Outline platelets.
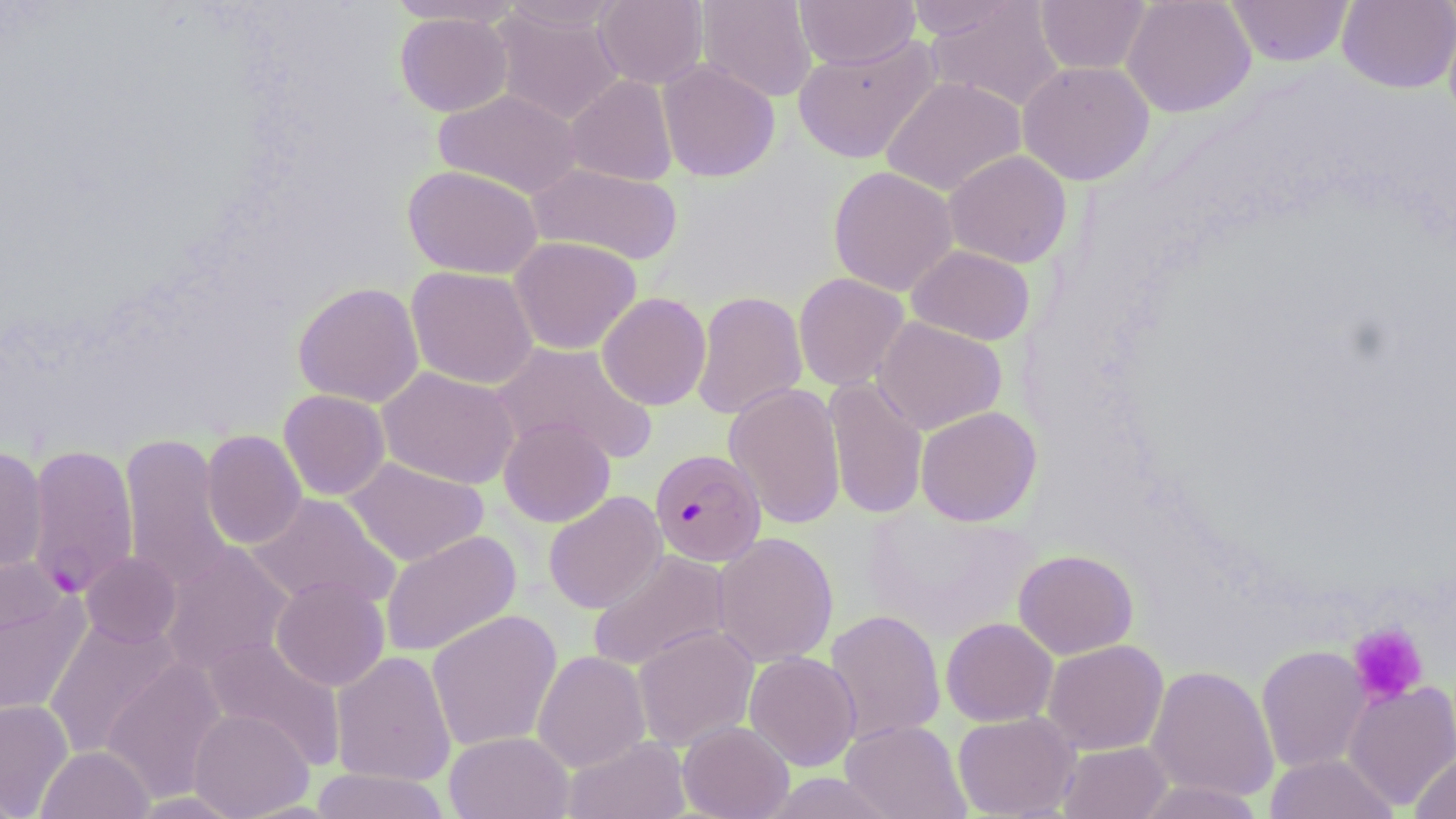
Approximate bounding boxes as [x1, y1, x2, y2] in pixels.
Platelets: [1347, 622, 1429, 706].

slide_level_diagnosis: Plasmodium falciparum
magnification: 1000x
image_size: 1456×819 pixels
modality: optical microscopy
field_of_view: one of a larger specimen
plasmodium_falciparum_infected_red_blood_cell_locations: 'approximate bounding boxes as [x1, y1, x2, y2] in pixels: [26, 443, 139, 597], [650, 448, 767, 566]'
stain: May-Grünwald-Giemsa
uninfected_red_blood_cell_locations: 'approximate bounding boxes as [x1, y1, x2, y2] in pixels: [385, 0, 523, 26], [593, 0, 708, 89], [696, 0, 817, 103], [794, 0, 920, 70], [904, 0, 1023, 40], [1034, 0, 1151, 75], [1121, 0, 1256, 117], [1225, 0, 1355, 67], [1337, 0, 1456, 94], [500, 1, 624, 31], [924, 1, 1066, 112], [490, 6, 624, 125], [395, 11, 513, 117], [792, 35, 942, 164], [657, 59, 780, 182], [1017, 60, 1155, 185], [565, 75, 678, 185], [881, 76, 1026, 196], [433, 88, 581, 198], [944, 150, 1072, 268], [526, 163, 684, 266], [403, 164, 542, 279], [828, 166, 958, 296], [509, 236, 642, 355], [907, 245, 1035, 345], [405, 266, 539, 389], [793, 272, 909, 391], [293, 282, 425, 407], [692, 290, 807, 421], [596, 292, 711, 410], [873, 316, 1007, 435], [491, 341, 658, 465], [377, 366, 521, 489], [824, 376, 928, 520], [724, 383, 847, 530], [278, 389, 390, 500], [915, 406, 1042, 527], [499, 417, 615, 527], [201, 430, 307, 550], [119, 433, 234, 592], [0, 445, 48, 573], [343, 457, 488, 567], [543, 491, 667, 614], [247, 492, 400, 611], [380, 530, 521, 657], [712, 531, 839, 668], [159, 543, 294, 675], [588, 548, 731, 673], [1013, 549, 1138, 659], [80, 551, 181, 648], [0, 553, 62, 649], [270, 576, 390, 691], [0, 596, 89, 719], [427, 609, 562, 753], [825, 609, 946, 745], [43, 617, 181, 760], [941, 617, 1058, 727], [633, 625, 759, 750], [202, 636, 347, 769], [1042, 640, 1168, 755], [1256, 645, 1371, 773], [332, 650, 456, 786], [532, 650, 650, 772], [744, 651, 861, 771], [101, 658, 228, 803], [1146, 664, 1279, 803], [1342, 680, 1456, 811], [0, 699, 74, 816], [189, 708, 313, 818], [952, 711, 1080, 819], [841, 719, 970, 819], [677, 721, 794, 819], [444, 731, 573, 819], [562, 735, 692, 819], [1057, 741, 1172, 819], [37, 746, 154, 819], [1409, 751, 1456, 819], [1264, 753, 1398, 819], [310, 768, 451, 819], [1132, 780, 1267, 819]'
preparation: thin blood smear